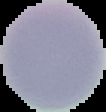 Cell region segmented out of the field of view; the surrounding area is masked to black. Image is 106×112 pixels. Malaria status: uninfected. From a thin blood smear.